Locate every Plasmodium parasite.
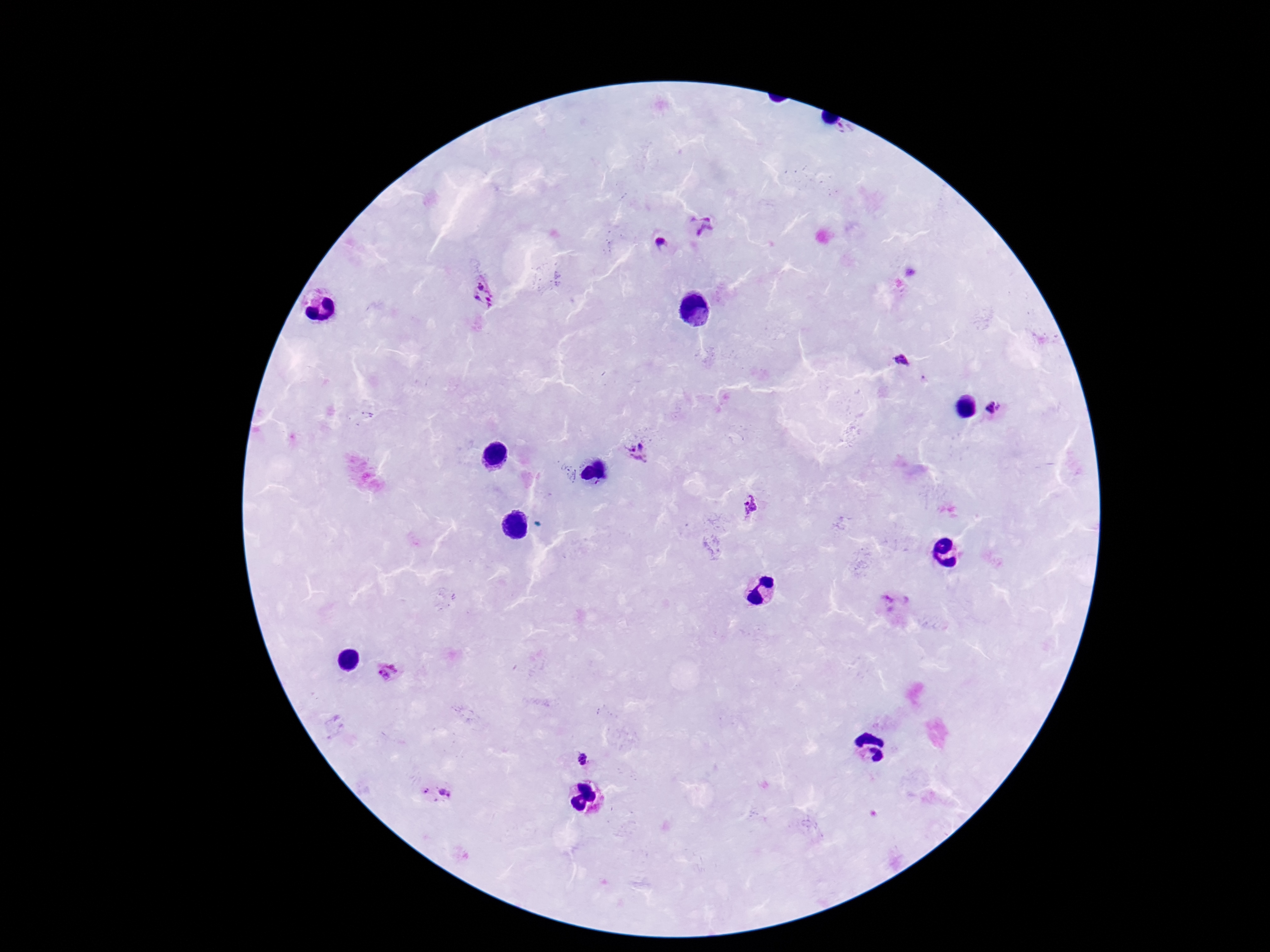
Approximate centers as {x, y} in pixels.
Plasmodium parasites: {704, 225}, {663, 243}, {480, 286}, {477, 298}, {493, 299}, {901, 362}, {997, 409}, {639, 454}, {754, 508}, {895, 601}, {387, 671}, {582, 759}, {446, 794}.

{
  "stain": "Giemsa",
  "patient_malaria_status": "infected",
  "image_size": "1270×952 pixels",
  "field_of_view": "one from this slide",
  "preparation": "thick peripheral-blood smear",
  "capture": "smartphone camera through the microscope eyepiece",
  "magnification": "100x"
}